Report the malaria status of this cell.
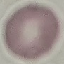
Uninfected.

stain = Giemsa
preparation = thin blood film
capture = smartphone camera at the microscope eyepiece
image type = automatically extracted cell patch, resized to 64 × 64 pixels